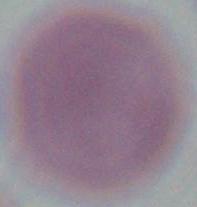

Micrograph. A red blood cell is seen. Captured at 1000x magnification.